Identify the parasite.
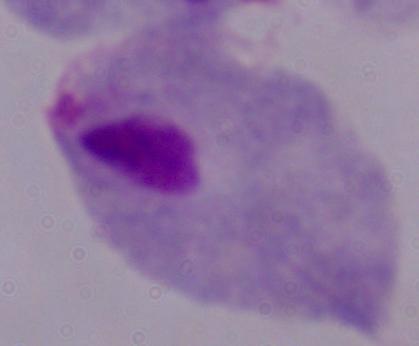

A trichomonad.

Summary:
  - Magnification: 1000x
  - Modality: micrograph